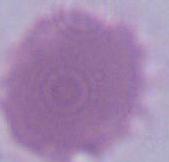
Photomicrograph. 1000x magnification. A red blood cell is shown.